Outline every parasitised red blood cell.
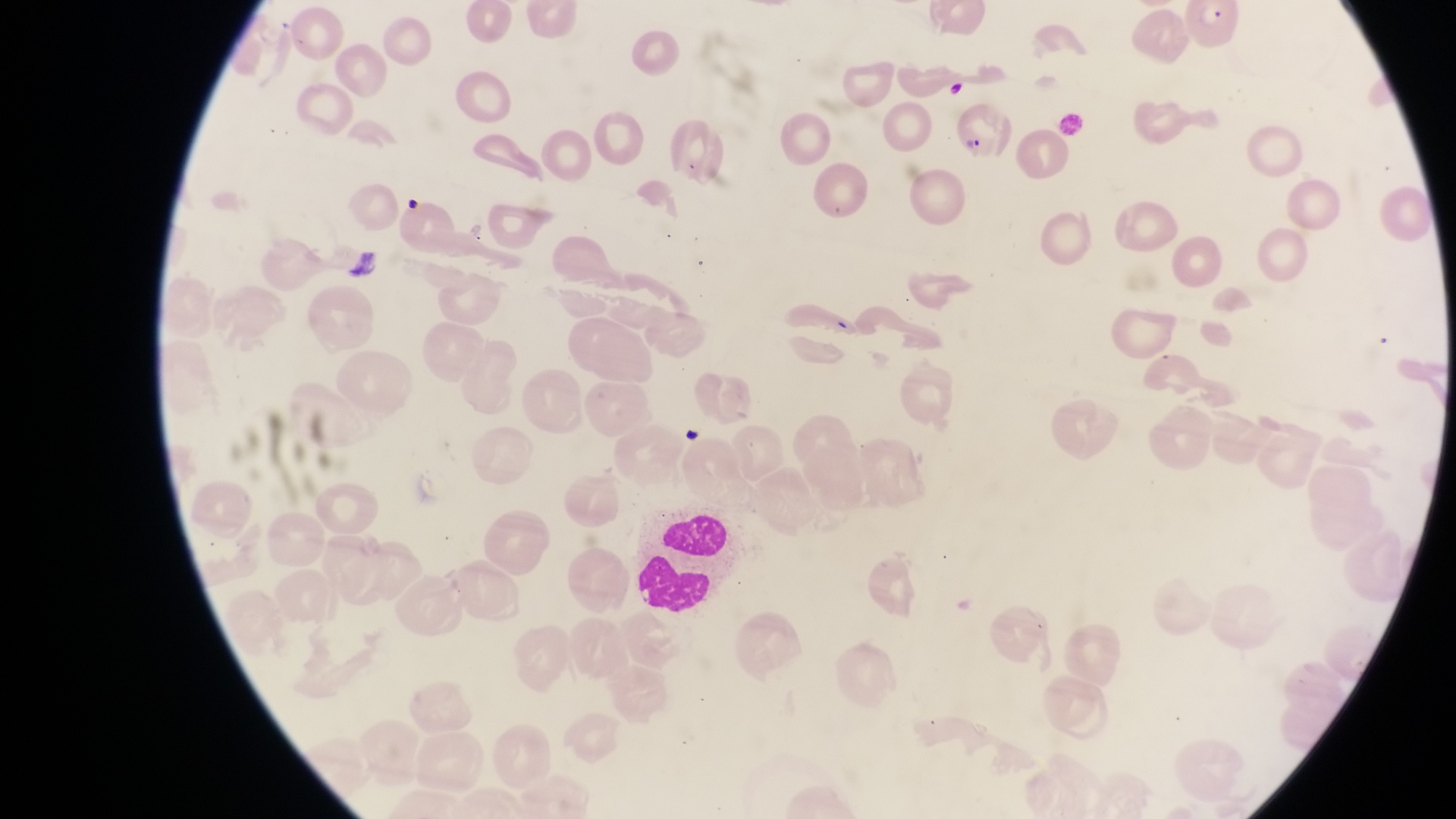
Approximate bounding boxes as [left, top, right, bottom] in pixels.
Parasitised red blood cells: [1182, 3, 1245, 53], [952, 111, 1010, 169].

Artifact (platelet-like body, stain precipitate, or debris) locations: [338, 243, 380, 279]. Leukocyte locations: [637, 510, 730, 612]. Sample from Uganda. Single field of view. Thin blood smear. Captured by a smartphone held over the eyepiece of an Olympus CX-23 microscope. At a magnification of 1000x. Image is 1456×819 pixels.